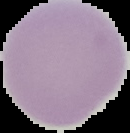

Summary:
  - Image type: segmented cell region with the area outside set to black
  - Result: no malaria parasites seen
  - Preparation: thin blood film
  - Image size: 130×133 pixels